Name the cell type shown.
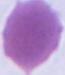

An erythrocyte.

Photomicrograph. 1000x magnification.